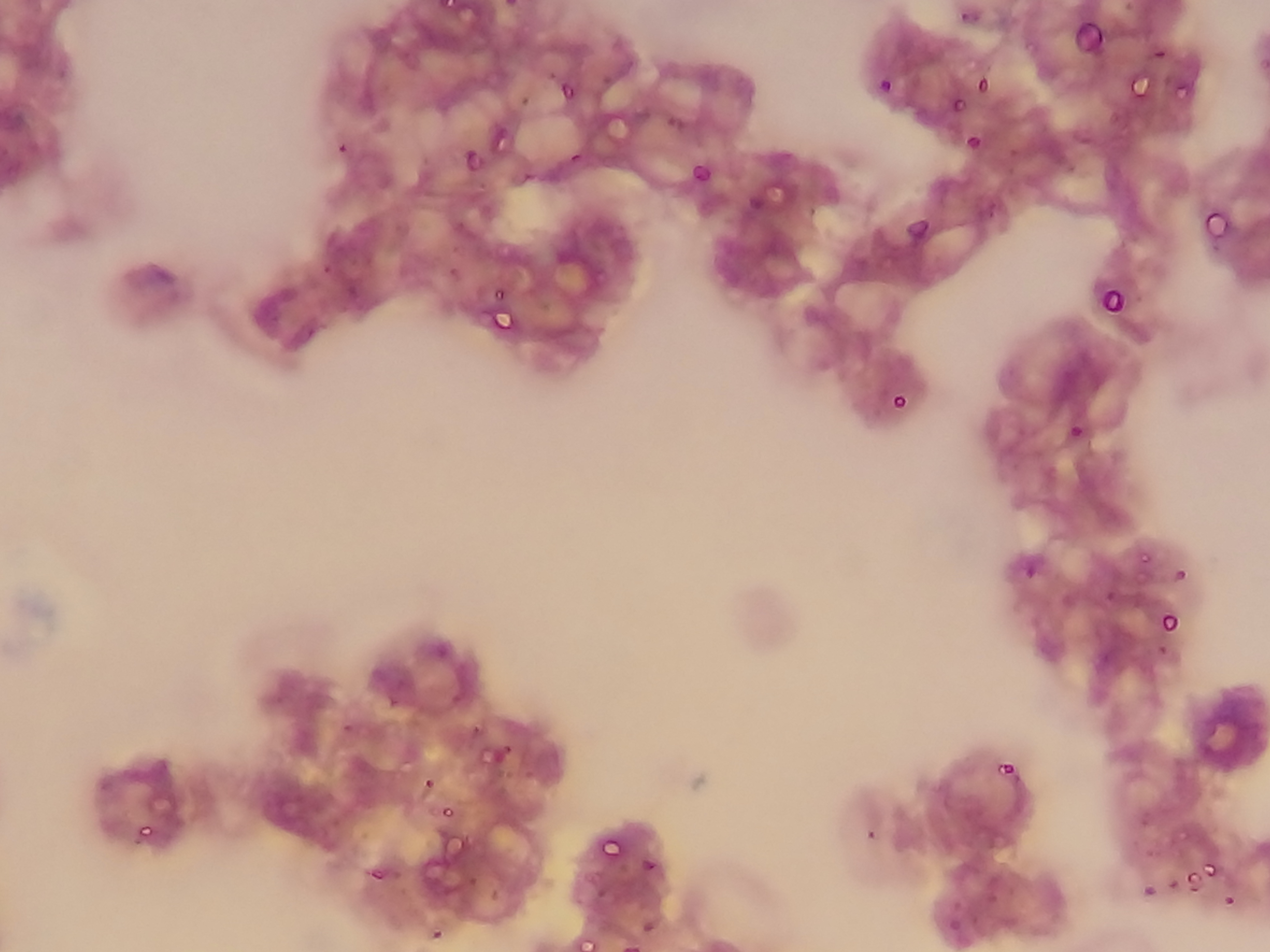

Approximate bounding boxes as [left, top, right, bottom] in pixels.
Summary:
  - Plasmodium parasite locations: [441, 0, 456, 12], [504, 0, 519, 9], [1063, 0, 1147, 45], [1121, 51, 1172, 92], [878, 76, 893, 94], [975, 76, 990, 93], [558, 79, 577, 102], [952, 97, 965, 112], [490, 127, 511, 148], [965, 132, 982, 149], [336, 141, 350, 155], [461, 149, 481, 169], [691, 161, 714, 183], [520, 169, 535, 184], [1202, 210, 1229, 238], [906, 216, 930, 239], [450, 244, 462, 256], [320, 263, 333, 276], [445, 264, 460, 280], [491, 285, 508, 304], [1101, 285, 1128, 312], [486, 299, 514, 328], [491, 310, 516, 333], [890, 392, 908, 410], [1068, 424, 1084, 439], [1139, 550, 1154, 567], [1021, 562, 1037, 580], [1173, 568, 1188, 583], [1106, 590, 1117, 602], [1158, 610, 1178, 634], [1156, 642, 1169, 655], [386, 697, 398, 709], [342, 720, 355, 735], [487, 740, 511, 764], [995, 760, 1016, 778], [424, 778, 436, 791], [439, 802, 456, 821], [134, 820, 157, 842], [865, 826, 878, 841], [596, 834, 624, 861], [641, 857, 658, 873], [1202, 862, 1220, 880], [365, 866, 383, 884], [1184, 870, 1200, 886], [1166, 880, 1178, 893], [1142, 883, 1155, 897], [487, 887, 501, 903], [1223, 895, 1236, 908], [948, 916, 962, 931], [641, 920, 656, 934], [429, 926, 445, 942]
  - Leukocyte locations: [732, 576, 799, 662]
  - Capture: mobile-phone photograph through a microscope
  - Field of view: single
  - Preparation: thin blood film
  - Country: Ghana
  - Image size: 1270×952 pixels